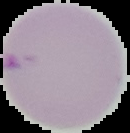
Summary:
  - Image size: 130×133 pixels
  - Image type: segmented cell region with the area outside set to black
  - Malaria status: uninfected
  - Preparation: thin blood smear